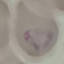

Summary:
  - Malaria status: parasitized
  - Capture: smartphone through the microscope eyepiece
  - Stain: Giemsa
  - Image type: cell patch, automatically extracted from a larger field of view and resized to 64 × 64 pixels
  - Preparation: thin smear